Name the parasite shown.
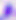

Toxoplasma gondii.

modality: photomicrograph
magnification: 400x